Identify the parasite.
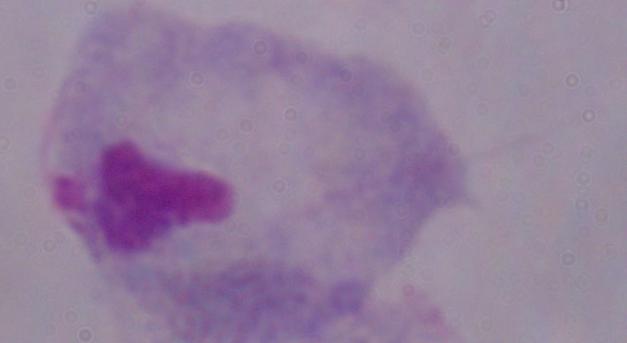

A trichomonad.

{
  "modality": "micrograph",
  "magnification": "1000x"
}